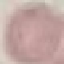
Result: no malaria parasites seen. Acquired by smartphone through the microscope eyepiece. Giemsa stain. Cell patch, automatically extracted from a larger field of view and resized to 64 × 64 pixels. Thin blood film.